State which parasite is depicted.
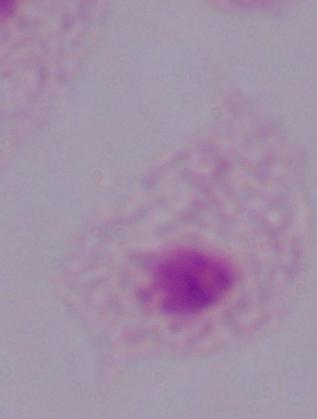

A trichomonad.

modality = micrograph
magnification = 1000x